Locate every Plasmodium falciparum-infected red blood cell.
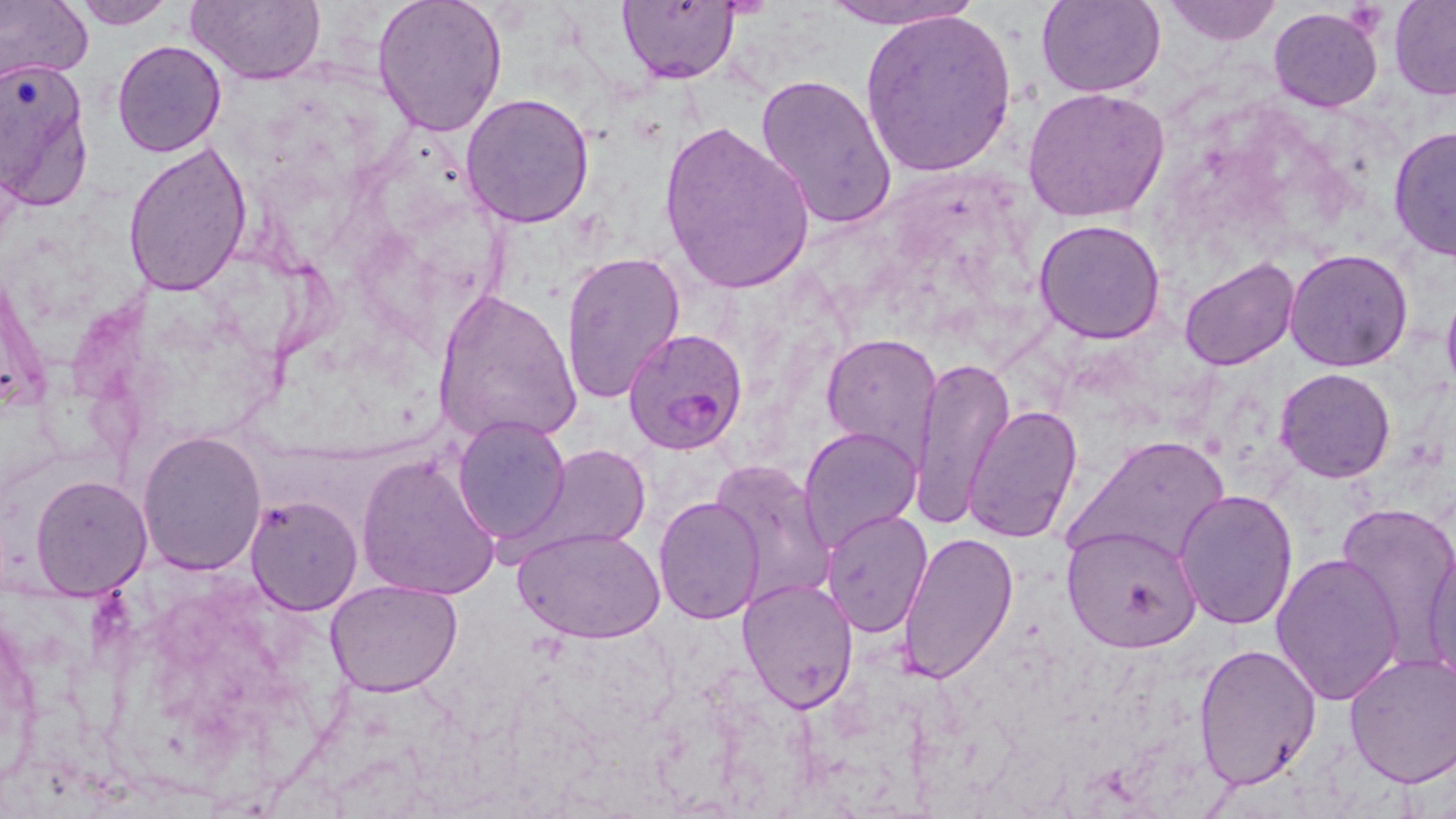
Approximate bounding boxes as (x1, y1, x2, y2) in pixels.
Plasmodium falciparum-infected red blood cells: (624, 327, 747, 454).

Summary:
  - Uninfected red blood cell locations: (0, 0, 93, 86), (65, 0, 175, 29), (185, 0, 326, 85), (619, 0, 741, 84), (812, 0, 987, 30), (1160, 0, 1283, 45), (1389, 0, 1456, 98), (371, 1, 510, 138), (1036, 1, 1166, 98), (1268, 7, 1384, 112), (859, 10, 1017, 177), (111, 40, 226, 158), (0, 61, 96, 213), (752, 73, 897, 230), (1023, 86, 1171, 223), (460, 92, 596, 229), (658, 119, 815, 294), (1389, 122, 1456, 262), (122, 141, 253, 297), (1034, 219, 1167, 343), (1285, 248, 1414, 372), (560, 252, 687, 406), (1178, 257, 1299, 371), (0, 260, 49, 417), (431, 287, 582, 446), (1440, 290, 1456, 396), (822, 333, 944, 466), (910, 355, 1014, 529), (1274, 366, 1396, 483), (964, 405, 1084, 544), (452, 416, 570, 544), (799, 426, 923, 554), (136, 430, 267, 575), (1070, 437, 1232, 569), (529, 443, 651, 553), (354, 452, 501, 600), (707, 457, 838, 610), (29, 474, 153, 600), (1172, 489, 1297, 631), (246, 494, 362, 615), (653, 495, 766, 624), (1335, 500, 1456, 659), (820, 509, 934, 635), (1062, 523, 1203, 653), (516, 528, 664, 645), (897, 528, 1019, 685), (1425, 529, 1456, 692), (1269, 551, 1405, 704), (737, 577, 859, 712), (323, 579, 464, 697), (1193, 642, 1321, 789), (1343, 652, 1456, 787)
  - Slide-level diagnosis: Plasmodium falciparum
  - Preparation: thin blood smear
  - Magnification: 1000x
  - Modality: light microscopy
  - Stain: May-Grünwald-Giemsa
  - Image size: 1456×819 pixels
  - Field of view: single